Outline each blood parasite and name the species.
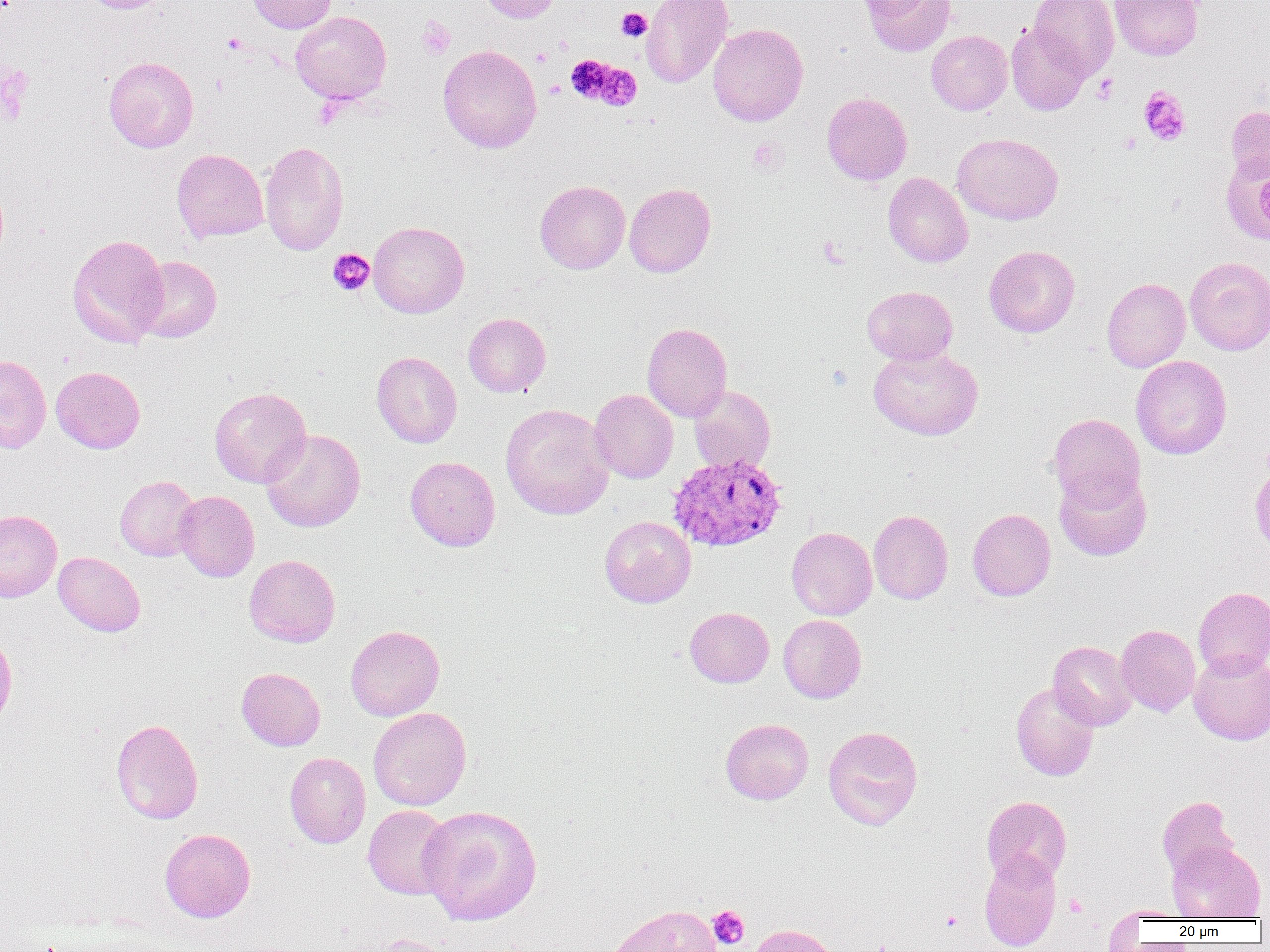

Approximate bounding boxes as (x1, y1, x2, y2) in pixels.
Plasmodium vivax-infected red blood cells: (668, 452, 788, 553).
No Plasmodium falciparum, Plasmodium ovale, Plasmodium malariae, Babesia divergens, or Trypanosoma brucei observed.

Summary:
  - Uninfected red blood cell locations: (81, 0, 174, 14), (246, 0, 337, 33), (477, 0, 563, 23), (640, 0, 734, 88), (862, 0, 957, 56), (1029, 0, 1119, 79), (1110, 0, 1203, 60), (291, 11, 392, 104), (1005, 22, 1090, 115), (707, 23, 808, 126), (926, 30, 1012, 115), (438, 44, 542, 153), (104, 57, 199, 152), (822, 92, 912, 185), (1226, 105, 1270, 182), (1223, 124, 1270, 248), (952, 133, 1063, 225), (260, 141, 349, 257), (171, 148, 269, 243), (883, 172, 973, 268), (535, 180, 630, 274), (624, 183, 716, 277), (368, 221, 469, 318), (67, 234, 169, 348), (983, 245, 1080, 337), (133, 256, 222, 343), (1184, 257, 1270, 355), (1102, 278, 1190, 372), (862, 285, 958, 365), (463, 313, 551, 397), (642, 322, 732, 421), (868, 346, 983, 440), (371, 351, 462, 448), (0, 355, 51, 453), (1131, 355, 1232, 459), (50, 366, 145, 454), (688, 385, 776, 474), (209, 386, 311, 488), (590, 389, 678, 484), (500, 403, 615, 520), (1048, 414, 1144, 510), (261, 429, 365, 532), (405, 455, 500, 552), (1054, 468, 1152, 562), (115, 476, 202, 562), (173, 491, 259, 582), (967, 508, 1056, 601), (0, 509, 62, 601), (868, 509, 953, 605), (599, 516, 695, 608), (786, 526, 877, 620), (53, 552, 145, 637), (244, 554, 341, 647), (1193, 586, 1270, 678), (685, 607, 774, 687), (778, 614, 866, 703), (345, 624, 444, 721), (1116, 624, 1200, 716), (0, 632, 17, 729), (1048, 641, 1136, 730), (1188, 650, 1270, 745), (236, 667, 325, 751), (1011, 682, 1100, 781), (368, 707, 471, 811), (720, 718, 813, 805), (111, 719, 203, 824), (823, 726, 923, 830), (284, 752, 370, 849), (982, 795, 1072, 885), (1157, 796, 1239, 880), (362, 804, 455, 900), (418, 804, 542, 926), (159, 828, 255, 923), (1167, 841, 1265, 921), (979, 850, 1061, 951), (605, 904, 724, 952), (1110, 905, 1191, 922), (747, 924, 842, 952), (371, 934, 467, 952)
  - Platelet locations: (616, 8, 652, 42), (417, 17, 455, 60), (222, 33, 248, 55), (533, 48, 552, 66), (565, 55, 631, 106), (0, 62, 33, 124), (1092, 74, 1118, 103), (1138, 85, 1191, 146), (1120, 133, 1141, 154), (748, 138, 786, 175), (818, 237, 849, 269), (328, 249, 374, 296), (708, 906, 749, 949), (941, 910, 963, 931)
  - Slide-level diagnosis: Plasmodium vivax
  - Preparation: thin blood smear
  - Image size: 1270×952 pixels
  - Modality: optical microscopy
  - Magnification: 1000x
  - Field of view: single